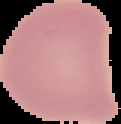

Summary:
  - Image type: cell region segmented out of the field of view; surrounding area masked to black
  - Image size: 121×124 pixels
  - Malaria status: uninfected
  - Preparation: thin blood film